Identify the cell.
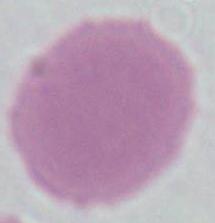

This is an erythrocyte.

Captured at 1000x magnification. Micrograph.